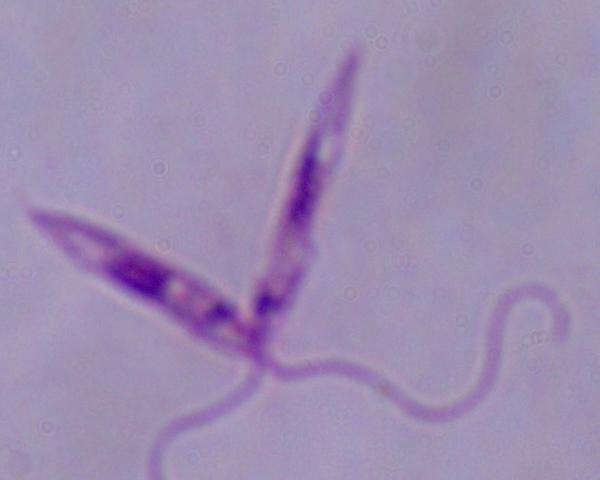

Summary:
  - Modality: micrograph
  - Magnification: 1000x
  - Identification: Leishmania